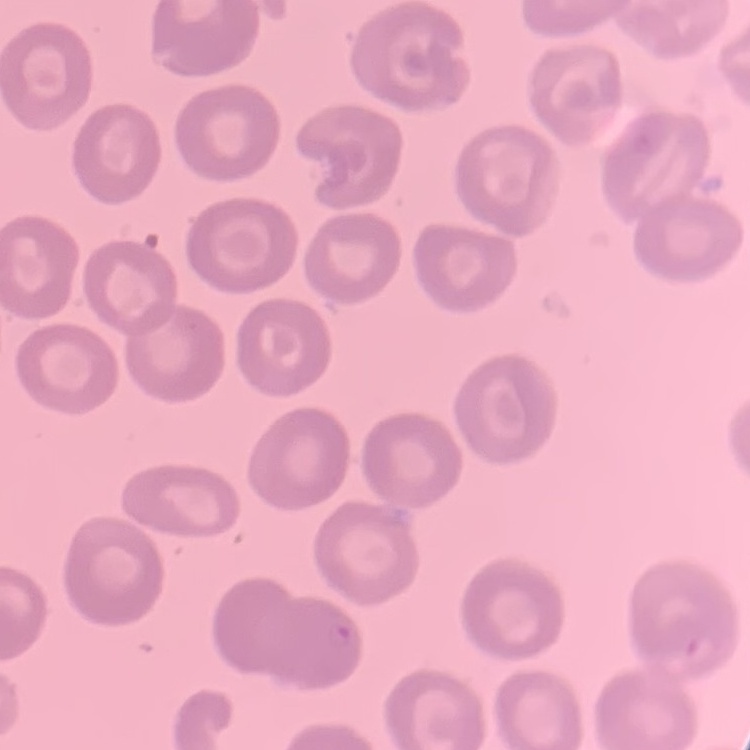
red blood cell morphology = no rouleaux formation
preparation = thin blood smear
image type = one tile cut from a larger photomicrograph
stain = Field's or Giemsa